Locate every Plasmodium ovale-infected red blood cell.
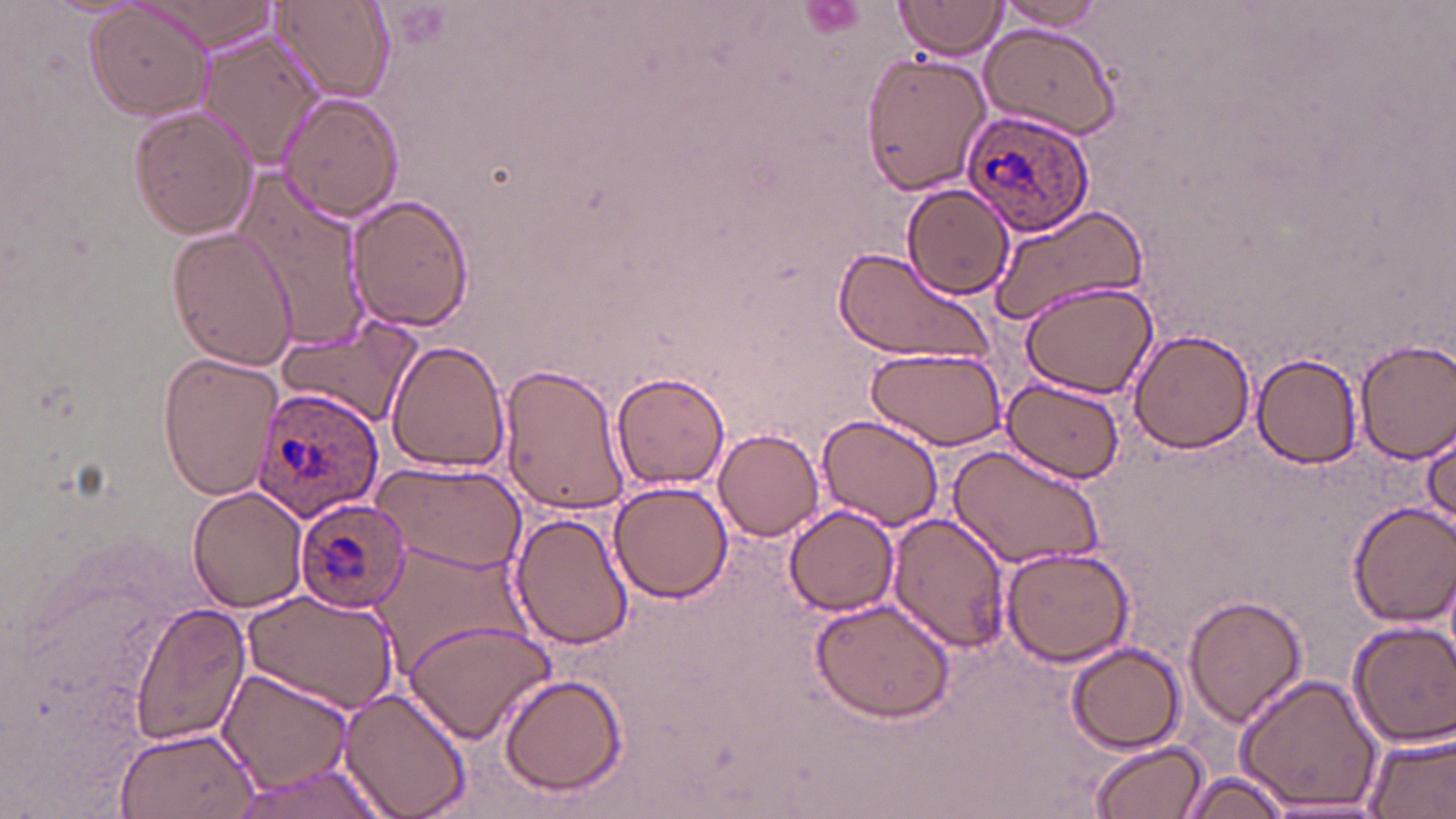

Approximate bounding boxes as (x1,y1)-(x2,y2) corner pairs in pixels.
Plasmodium ovale-infected red blood cells: (961,107)-(1100,238), (253,387)-(384,519), (294,497)-(411,614).

Uninfected red blood cell locations: (138,0)-(281,49), (276,0)-(394,103), (894,0)-(1011,62), (994,0)-(1114,33), (84,2)-(214,120), (977,23)-(1121,141), (196,29)-(321,168), (863,50)-(990,196), (279,93)-(404,223), (127,104)-(259,240), (228,171)-(372,347), (903,182)-(1012,300), (345,196)-(474,333), (986,202)-(1147,332), (165,227)-(300,370), (830,246)-(995,367), (1020,280)-(1157,398), (275,318)-(425,428), (1128,328)-(1256,455), (1355,338)-(1456,462), (384,339)-(511,474), (866,344)-(1009,451), (158,351)-(282,501), (1251,352)-(1364,469), (500,361)-(632,518), (611,372)-(730,489), (1002,376)-(1126,487), (816,412)-(947,533), (1422,420)-(1455,539), (713,427)-(825,543), (946,440)-(1109,573), (366,461)-(529,572), (606,480)-(732,606), (186,485)-(309,612), (1348,502)-(1455,627), (783,505)-(900,618), (509,510)-(637,651), (884,511)-(1010,650), (368,544)-(529,675), (1000,544)-(1137,667), (242,589)-(399,713), (1183,592)-(1307,728), (809,593)-(957,724), (128,604)-(252,746), (400,620)-(555,743), (1346,620)-(1456,748), (1064,641)-(1186,755), (217,666)-(353,794), (1235,672)-(1385,814), (497,674)-(627,796), (336,687)-(471,819), (112,726)-(259,819), (1364,728)-(1456,819), (1088,739)-(1210,818), (223,760)-(397,819), (1181,770)-(1297,818), (1253,798)-(1394,818). Slide-level diagnosis: Plasmodium ovale. May-Grünwald-Giemsa stain. Single field of view. Thin blood film. 1000x magnification. Image is 1456×819 pixels. Light microscopy.